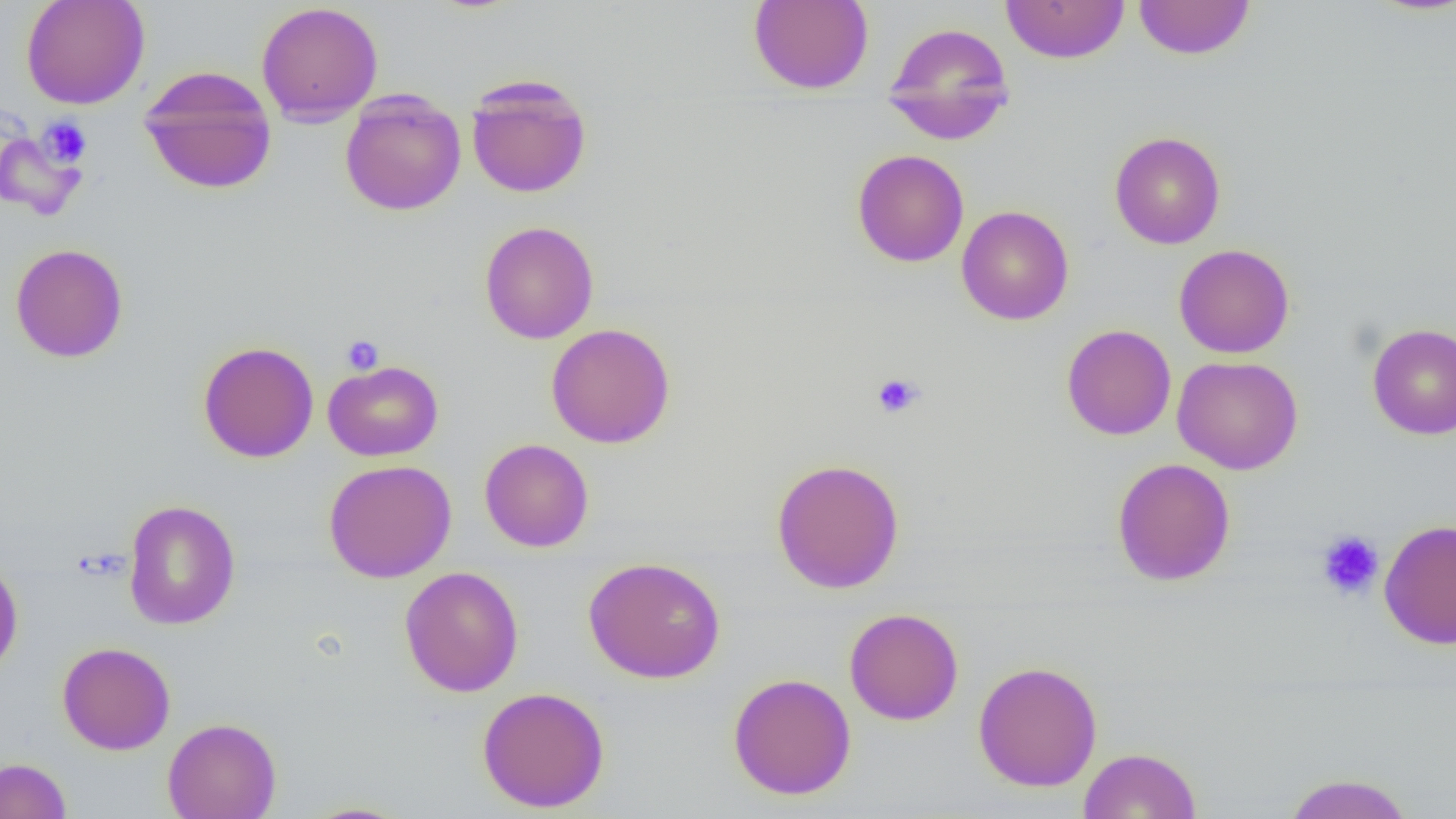
{
  "slide_level_diagnosis": "no evidence of blood parasites",
  "magnification": "1000x",
  "field_of_view": "single",
  "preparation": "thin blood film",
  "modality": "optical microscopy",
  "platelet_locations": "approximate bounding boxes as [x1, y1, x2, y2] in pixels: [38, 116, 92, 167], [341, 334, 384, 375], [871, 372, 924, 419], [1315, 530, 1384, 601]",
  "image_size": "1456×819 pixels",
  "uninfected_red_blood_cell_locations": "approximate bounding boxes as [x1, y1, x2, y2] in pixels: [21, 0, 151, 110], [749, 0, 874, 94], [1000, 0, 1130, 64], [1134, 0, 1255, 60], [256, 2, 383, 125], [882, 21, 1015, 143], [139, 66, 277, 195], [465, 75, 592, 199], [340, 90, 466, 216], [1110, 131, 1226, 250], [852, 149, 969, 268], [956, 205, 1074, 325], [479, 221, 599, 344], [10, 243, 128, 363], [1174, 243, 1295, 358], [1367, 322, 1456, 440], [546, 323, 676, 448], [1061, 324, 1177, 440], [198, 341, 319, 462], [1171, 356, 1303, 475], [323, 360, 444, 461], [479, 438, 594, 553], [771, 457, 905, 594], [1112, 458, 1236, 586], [323, 459, 456, 582], [122, 500, 241, 629], [1379, 519, 1456, 650], [583, 556, 726, 684], [0, 557, 24, 679], [399, 566, 524, 697], [844, 608, 964, 725], [58, 642, 175, 755], [973, 660, 1103, 792], [727, 672, 856, 800], [477, 686, 610, 813], [162, 717, 282, 819], [1079, 747, 1201, 819], [0, 757, 71, 819], [1282, 772, 1415, 818], [298, 801, 414, 819]"
}